Outline every Plasmodium parasite.
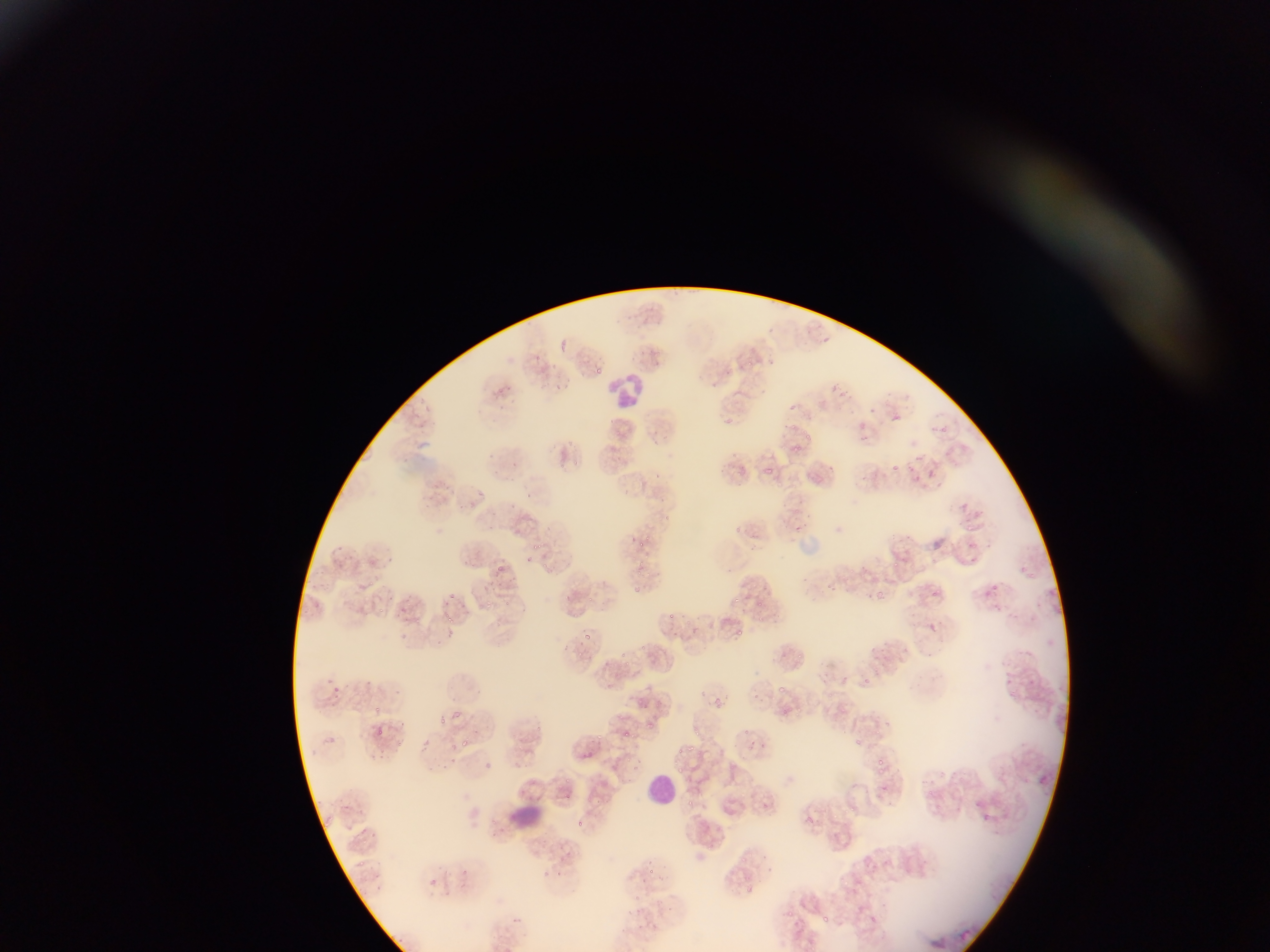

Approximate bounding boxes as left top right bottom in pixels.
Plasmodium parasites: 813 321 825 332; 823 335 832 344; 561 339 569 358; 769 357 777 366; 747 360 753 369; 592 363 603 378; 549 379 564 393; 494 384 514 395; 831 384 840 393; 839 390 848 399; 792 403 796 412; 868 407 874 416; 892 413 902 425; 786 420 797 434; 936 425 950 435; 807 430 814 444; 862 434 872 442; 791 441 804 453; 914 455 922 462; 569 456 579 470; 511 460 520 468; 558 462 570 470; 828 464 837 472; 891 464 899 473; 763 465 779 483; 909 466 919 474; 928 470 936 480; 938 480 945 489; 478 491 486 499; 962 503 969 512; 975 511 985 518; 962 521 982 536; 644 533 661 545; 633 535 645 547; 531 539 550 553; 525 553 541 570; 634 557 653 574; 891 557 914 579; 543 561 555 571; 489 562 506 576; 1021 565 1035 581; 368 581 375 590; 990 582 1000 593; 632 583 653 598; 828 585 844 595; 870 588 885 601; 1050 588 1057 597; 932 589 942 599; 443 592 457 603; 480 594 496 608; 561 594 571 604; 729 594 740 606; 500 596 515 611; 581 597 593 608; 754 600 766 611; 379 603 390 622; 993 604 1002 614; 409 609 428 633; 442 610 458 625; 665 612 678 622; 924 621 940 636; 736 629 750 643; 584 630 594 641; 639 642 648 654; 621 649 638 665; 792 649 805 662; 857 673 872 689; 776 682 791 697; 332 683 347 703; 710 694 729 714; 634 697 646 709; 781 702 788 716; 372 704 385 719; 795 704 808 718; 438 716 448 727; 645 717 661 736; 535 724 543 737; 740 727 752 736; 373 729 392 743; 594 729 605 744; 693 730 703 739; 625 732 635 742; 326 735 336 743; 461 738 473 751; 392 740 406 750; 420 740 437 758; 687 741 696 758; 676 746 688 754; 626 752 643 770; 873 757 882 767; 677 764 688 777; 875 767 890 777; 565 778 570 786; 925 786 938 801; 564 793 577 800; 688 798 695 808; 849 804 862 815; 831 810 841 824; 982 813 990 821; 805 814 816 824; 578 820 588 830; 558 847 577 864; 740 856 752 865; 458 865 478 884; 648 866 656 874; 554 873 564 883; 423 874 446 892; 840 875 851 889; 744 884 754 893; 787 911 795 916; 819 913 832 923 | approximate x y pixel centers of objects too small to bound: 797 527.

field_of_view: single
leukocyte_locations: 'approximate bounding boxes as left top right bottom in pixels: 613 374 641 409; 646 772 676 804; 511 805 543 824'
country: Ghana
image_size: 1270×952 pixels
preparation: thin blood smear
capture: mobile-phone photograph through a microscope